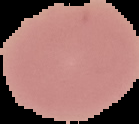
Image is 139×124 pixels. Malaria status: uninfected. Cell region segmented out of the field of view; the surrounding area is masked to black. From a thin blood smear.